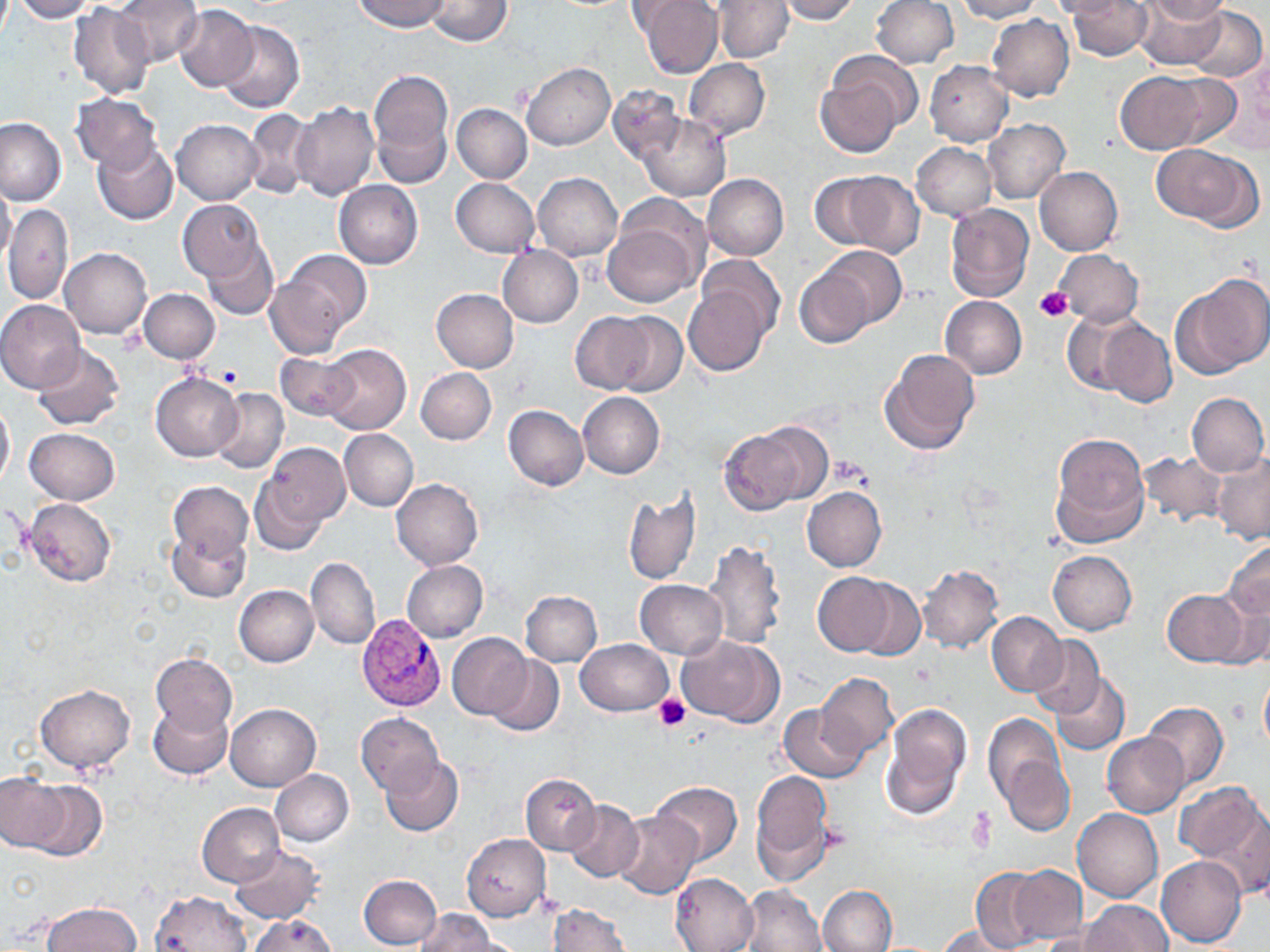

slide-level diagnosis = Plasmodium vivax
field of view = one of a larger specimen
Plasmodium vivax-infected red blood cell locations = approximate bounding boxes as named x1/y1/x2/y2 corners in pixels: (x1=357, y1=614, x2=448, y2=711)
image size = 1270×952 pixels
uninfected red blood cell locations = approximate bounding boxes as named x1/y1/x2/y2 corners in pixels: (x1=0, y1=0, x2=11, y2=40), (x1=12, y1=0, x2=99, y2=22), (x1=113, y1=0, x2=204, y2=68), (x1=354, y1=0, x2=448, y2=32), (x1=423, y1=0, x2=513, y2=46), (x1=634, y1=0, x2=723, y2=79), (x1=775, y1=0, x2=864, y2=24), (x1=870, y1=0, x2=960, y2=69), (x1=1051, y1=0, x2=1131, y2=19), (x1=1132, y1=0, x2=1230, y2=71), (x1=1141, y1=0, x2=1231, y2=25), (x1=951, y1=1, x2=1046, y2=23), (x1=1063, y1=1, x2=1155, y2=61), (x1=716, y1=2, x2=797, y2=61), (x1=69, y1=4, x2=155, y2=98), (x1=174, y1=5, x2=258, y2=91), (x1=1189, y1=7, x2=1265, y2=82), (x1=985, y1=13, x2=1074, y2=100), (x1=218, y1=22, x2=304, y2=113), (x1=825, y1=52, x2=922, y2=139), (x1=684, y1=58, x2=771, y2=141), (x1=925, y1=60, x2=1014, y2=146), (x1=521, y1=62, x2=615, y2=150), (x1=367, y1=68, x2=455, y2=184), (x1=1113, y1=68, x2=1232, y2=156), (x1=815, y1=79, x2=903, y2=156), (x1=609, y1=82, x2=685, y2=164), (x1=71, y1=94, x2=163, y2=172), (x1=291, y1=102, x2=380, y2=202), (x1=451, y1=104, x2=531, y2=183), (x1=245, y1=109, x2=313, y2=199), (x1=634, y1=114, x2=730, y2=203), (x1=0, y1=116, x2=68, y2=206), (x1=173, y1=120, x2=263, y2=204), (x1=983, y1=120, x2=1069, y2=204), (x1=93, y1=138, x2=180, y2=225), (x1=912, y1=142, x2=998, y2=220), (x1=1150, y1=144, x2=1259, y2=226), (x1=1034, y1=166, x2=1124, y2=255), (x1=815, y1=167, x2=925, y2=258), (x1=533, y1=173, x2=623, y2=261), (x1=702, y1=173, x2=789, y2=260), (x1=452, y1=177, x2=540, y2=257), (x1=333, y1=180, x2=423, y2=268), (x1=0, y1=182, x2=16, y2=268), (x1=616, y1=191, x2=710, y2=274), (x1=180, y1=199, x2=263, y2=281), (x1=945, y1=203, x2=1035, y2=303), (x1=3, y1=205, x2=73, y2=306), (x1=604, y1=225, x2=699, y2=306), (x1=206, y1=242, x2=278, y2=320), (x1=497, y1=246, x2=584, y2=327), (x1=794, y1=246, x2=905, y2=348), (x1=60, y1=248, x2=152, y2=337), (x1=1055, y1=248, x2=1144, y2=326), (x1=270, y1=249, x2=371, y2=353), (x1=697, y1=254, x2=785, y2=340), (x1=1175, y1=273, x2=1266, y2=376), (x1=685, y1=279, x2=773, y2=376), (x1=139, y1=288, x2=220, y2=363), (x1=432, y1=288, x2=519, y2=372), (x1=941, y1=296, x2=1028, y2=380), (x1=0, y1=299, x2=85, y2=392), (x1=1061, y1=308, x2=1144, y2=395), (x1=608, y1=312, x2=685, y2=395), (x1=571, y1=313, x2=652, y2=392), (x1=1100, y1=318, x2=1177, y2=407), (x1=318, y1=343, x2=412, y2=435), (x1=31, y1=344, x2=124, y2=431), (x1=879, y1=348, x2=981, y2=457), (x1=276, y1=353, x2=360, y2=420), (x1=416, y1=367, x2=497, y2=444), (x1=151, y1=374, x2=244, y2=461), (x1=166, y1=374, x2=280, y2=497), (x1=210, y1=388, x2=288, y2=475), (x1=579, y1=392, x2=665, y2=478), (x1=1187, y1=392, x2=1268, y2=475), (x1=0, y1=396, x2=14, y2=494), (x1=504, y1=406, x2=589, y2=491), (x1=717, y1=423, x2=823, y2=516), (x1=25, y1=427, x2=121, y2=505), (x1=338, y1=429, x2=418, y2=510), (x1=1050, y1=434, x2=1149, y2=549), (x1=261, y1=441, x2=350, y2=533), (x1=1139, y1=450, x2=1226, y2=531), (x1=1211, y1=452, x2=1270, y2=544), (x1=251, y1=469, x2=334, y2=557), (x1=391, y1=478, x2=483, y2=570), (x1=168, y1=482, x2=254, y2=558), (x1=622, y1=486, x2=704, y2=589), (x1=803, y1=486, x2=887, y2=571), (x1=24, y1=499, x2=116, y2=588), (x1=169, y1=528, x2=250, y2=602), (x1=702, y1=539, x2=786, y2=652), (x1=1222, y1=540, x2=1270, y2=633), (x1=1047, y1=549, x2=1138, y2=635), (x1=306, y1=557, x2=380, y2=651), (x1=402, y1=559, x2=489, y2=641), (x1=918, y1=565, x2=1004, y2=654), (x1=813, y1=572, x2=901, y2=657), (x1=853, y1=577, x2=926, y2=661), (x1=634, y1=580, x2=726, y2=658), (x1=235, y1=585, x2=319, y2=667), (x1=1162, y1=589, x2=1250, y2=667), (x1=521, y1=590, x2=601, y2=666), (x1=987, y1=613, x2=1066, y2=695), (x1=446, y1=632, x2=532, y2=719), (x1=678, y1=635, x2=780, y2=723), (x1=1028, y1=636, x2=1105, y2=718), (x1=577, y1=638, x2=673, y2=716), (x1=151, y1=654, x2=237, y2=736), (x1=490, y1=656, x2=564, y2=737), (x1=817, y1=671, x2=898, y2=760), (x1=1259, y1=671, x2=1270, y2=755), (x1=1051, y1=673, x2=1131, y2=755), (x1=36, y1=685, x2=135, y2=774), (x1=148, y1=700, x2=234, y2=779), (x1=1144, y1=700, x2=1229, y2=792), (x1=779, y1=703, x2=866, y2=783), (x1=880, y1=703, x2=970, y2=820), (x1=227, y1=704, x2=320, y2=790), (x1=357, y1=713, x2=445, y2=797), (x1=984, y1=715, x2=1075, y2=835), (x1=1104, y1=733, x2=1187, y2=817), (x1=381, y1=755, x2=464, y2=836), (x1=270, y1=768, x2=354, y2=846), (x1=752, y1=769, x2=833, y2=875), (x1=2, y1=773, x2=96, y2=858), (x1=521, y1=773, x2=599, y2=854), (x1=651, y1=781, x2=743, y2=865), (x1=1177, y1=781, x2=1266, y2=887), (x1=565, y1=799, x2=644, y2=881), (x1=197, y1=803, x2=283, y2=887), (x1=1072, y1=805, x2=1162, y2=902), (x1=613, y1=811, x2=703, y2=899), (x1=462, y1=833, x2=551, y2=921), (x1=231, y1=845, x2=324, y2=924), (x1=1157, y1=853, x2=1247, y2=946), (x1=1009, y1=865, x2=1087, y2=945), (x1=971, y1=867, x2=1041, y2=951), (x1=359, y1=874, x2=441, y2=949), (x1=671, y1=874, x2=760, y2=952), (x1=817, y1=884, x2=898, y2=952), (x1=737, y1=885, x2=827, y2=952), (x1=151, y1=891, x2=252, y2=952), (x1=1078, y1=900, x2=1173, y2=952), (x1=40, y1=902, x2=143, y2=952), (x1=547, y1=905, x2=630, y2=952), (x1=414, y1=909, x2=504, y2=950), (x1=245, y1=913, x2=340, y2=952), (x1=933, y1=925, x2=1016, y2=952)
preparation = thin blood film
modality = optical microscopy
magnification = 1000x
platelet locations = approximate bounding boxes as named x1/y1/x2/y2 corners in pixels: (x1=1035, y1=286, x2=1073, y2=324), (x1=218, y1=365, x2=241, y2=387), (x1=827, y1=456, x2=875, y2=490), (x1=653, y1=692, x2=693, y2=733)
stain = May-Grünwald-Giemsa